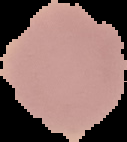

Summary:
  - Image size: 127×142 pixels
  - Result: no Plasmodium parasites detected
  - Preparation: thin blood film
  - Image type: segmented cell region with the area outside set to black